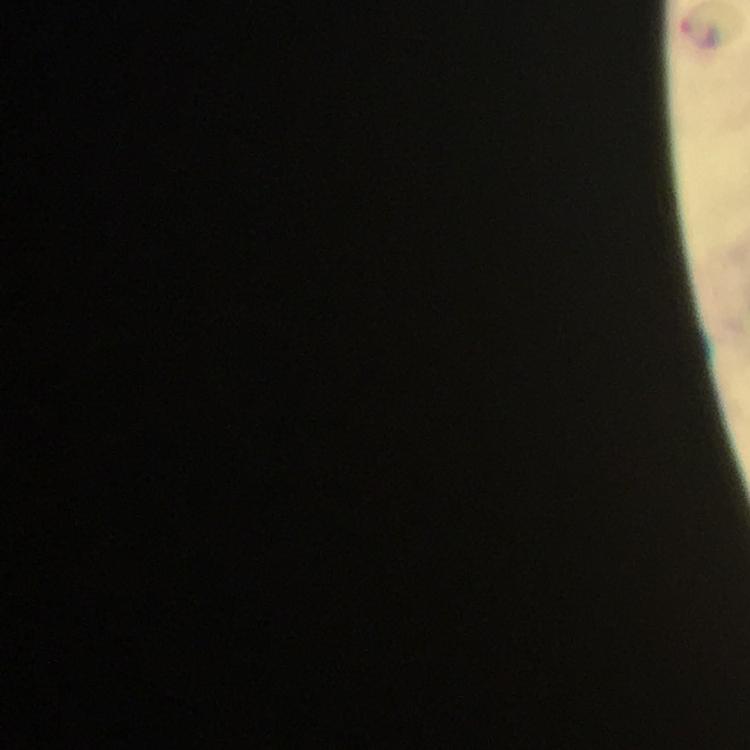
Approximate centers as (x, y) in pixels. Malaria parasite locations: (702, 31). Photographed with a smartphone mounted on the microscope. Giemsa stain. Immersion oil applied. Image is 750×750 pixels. From a malaria diagnostic workup. A crop from one field of view. At 100x magnification. Thick blood smear.